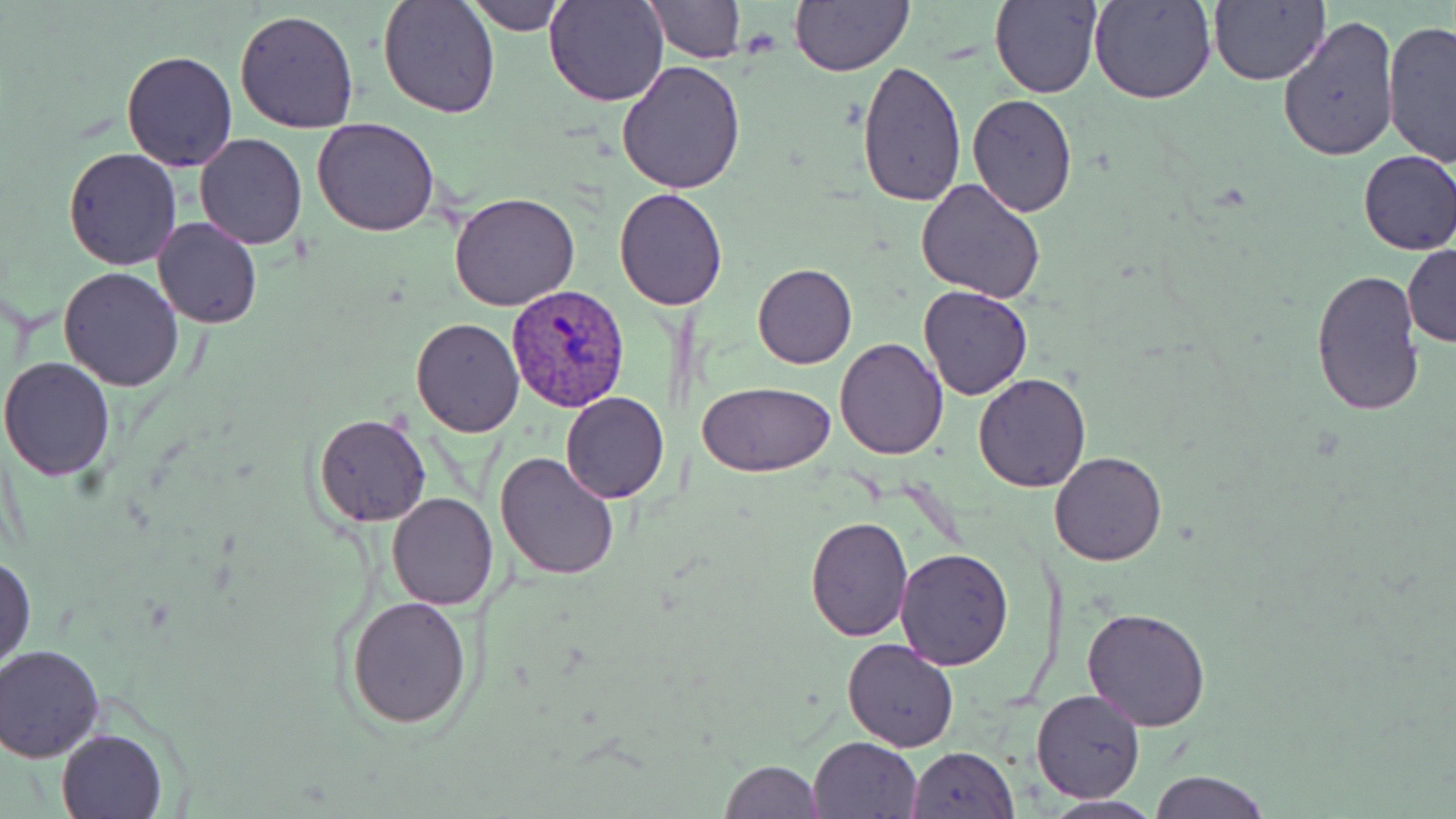
plasmodium_vivax_infected_red_blood_cell_locations: 'approximate bounding boxes as (x1,y1)-(x2,y2) corner pairs in pixels: (506,285)-(631,412)'
slide_level_diagnosis: Plasmodium vivax
magnification: 1000x
uninfected_red_blood_cell_locations: 'approximate bounding boxes as (x1,y1)-(x2,y2) corner pairs in pixels: (377,0)-(500,119), (463,0)-(567,34), (544,0)-(670,106), (644,0)-(745,62), (991,0)-(1102,100), (1089,0)-(1216,105), (1208,0)-(1328,85), (790,1)-(912,75), (234,9)-(361,133), (1277,15)-(1400,162), (1381,18)-(1456,164), (120,49)-(236,171), (616,59)-(750,194), (857,59)-(968,207), (967,94)-(1078,216), (312,118)-(441,237), (193,133)-(307,251), (62,147)-(182,269), (1356,150)-(1456,256), (914,179)-(1046,303), (612,188)-(731,310), (449,192)-(580,311), (153,217)-(262,328), (1403,243)-(1456,348), (753,262)-(857,368), (59,266)-(183,392), (1310,269)-(1427,417), (918,286)-(1034,400), (410,318)-(525,438), (835,337)-(949,459), (0,356)-(118,480), (972,373)-(1091,492), (696,379)-(836,475), (560,392)-(669,504), (313,414)-(432,526), (493,449)-(621,579), (1050,451)-(1167,566), (387,492)-(498,609), (803,516)-(914,640), (895,547)-(1013,669), (0,554)-(35,671), (345,595)-(475,729), (1082,606)-(1210,731), (842,637)-(959,752), (1,644)-(104,760), (1031,689)-(1144,803), (56,729)-(165,818), (809,736)-(923,819), (904,747)-(1018,819), (718,759)-(825,818), (1150,770)-(1270,819), (1039,795)-(1164,817)'
field_of_view: single
preparation: thin blood smear
modality: light microscopy
image_size: 1456×819 pixels
stain: May-Grünwald-Giemsa